Describe the morphology of the red blood cells.
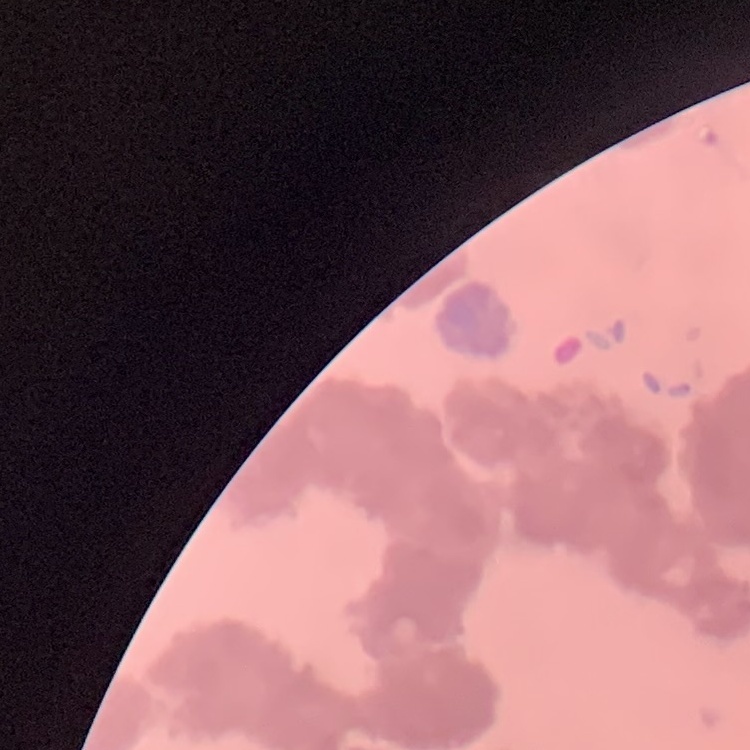
They show rouleaux formation.

One tile cut from a larger photomicrograph. Field's or Giemsa stain. Thin peripheral smear.